State which parasite is depicted.
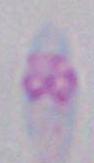
This is Toxoplasma gondii.

Summary:
  - Modality: photomicrograph
  - Magnification: 1000x